Identify the parasite.
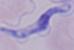

A trypanosome.

magnification = 1000x
modality = micrograph